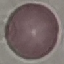

Result: no malaria parasites seen. Cell patch, automatically extracted from a larger field of view and resized to 64 × 64 pixels. Thin blood film. Giemsa-stained preparation. Acquired by smartphone through the microscope eyepiece.